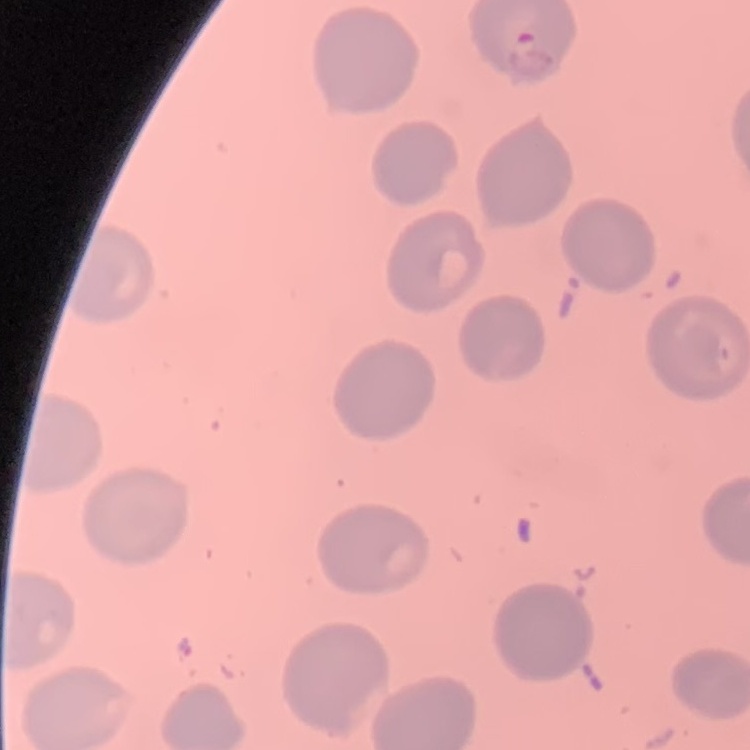
Summary:
  - Red blood cell morphology: no rouleaux formation
  - Image type: one tile cut from a larger photomicrograph
  - Stain: Field's or Giemsa
  - Preparation: thin peripheral smear